Assess this cell for malaria.
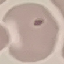
It is uninfected.

Thin blood smear. Acquired by smartphone through the microscope eyepiece. Giemsa-stained preparation. Cell patch, automatically extracted from a larger field of view and resized to 64 × 64 pixels.